Look for Plasmodium parasites.
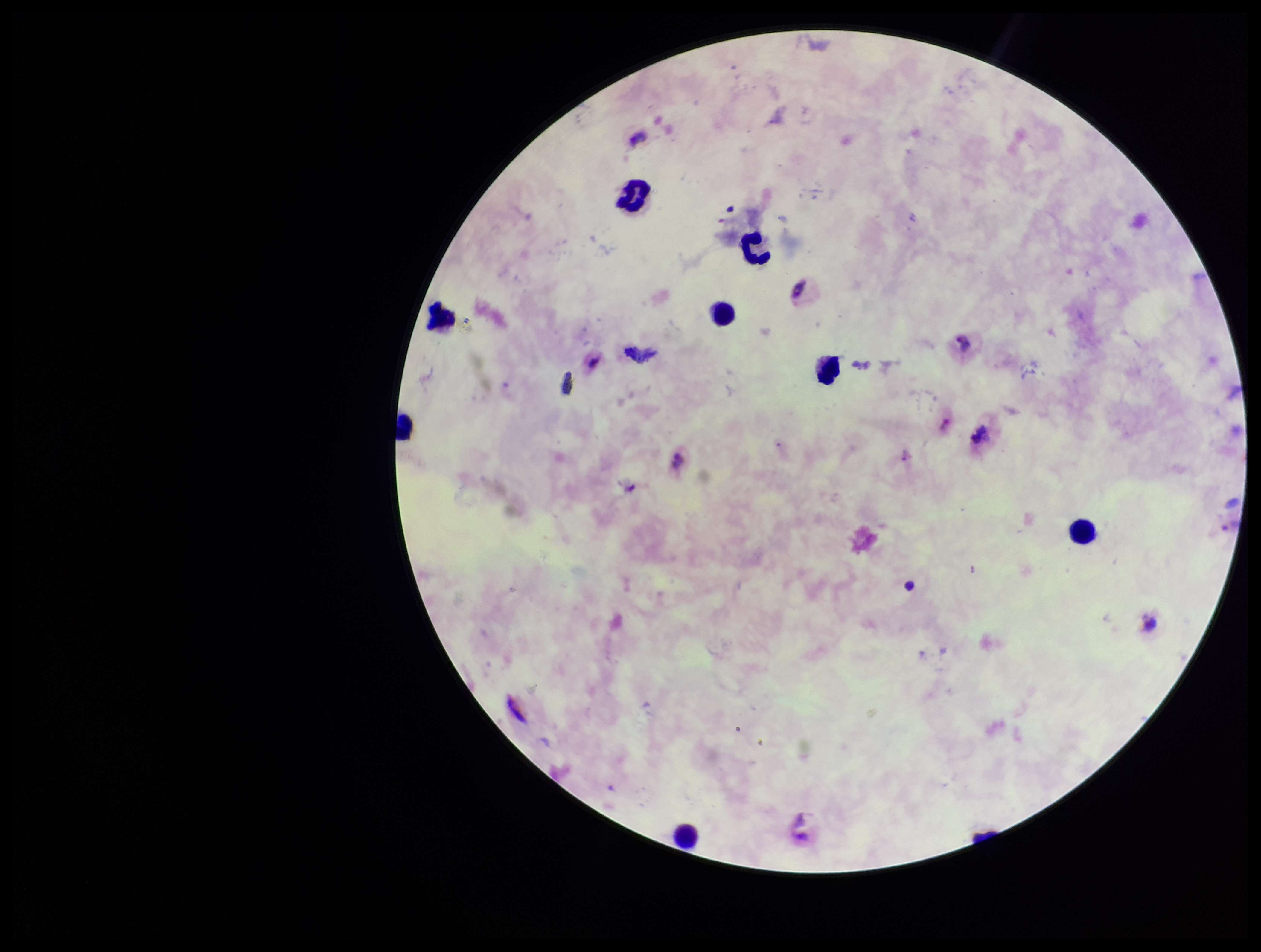
Identified.

Summary:
  - Field of view: one from this slide
  - Species reported for this patient: Plasmodium vivax
  - Patient malaria status: infected
  - Stain: Giemsa
  - Preparation: thick smear
  - Capture: smartphone photograph through the microscope eyepiece
  - Parasite count: 1
  - Image size: 1261×952 pixels
  - Leukocyte count: 8